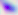

Summary:
  - Identification: Toxoplasma gondii
  - Modality: micrograph
  - Magnification: 400x